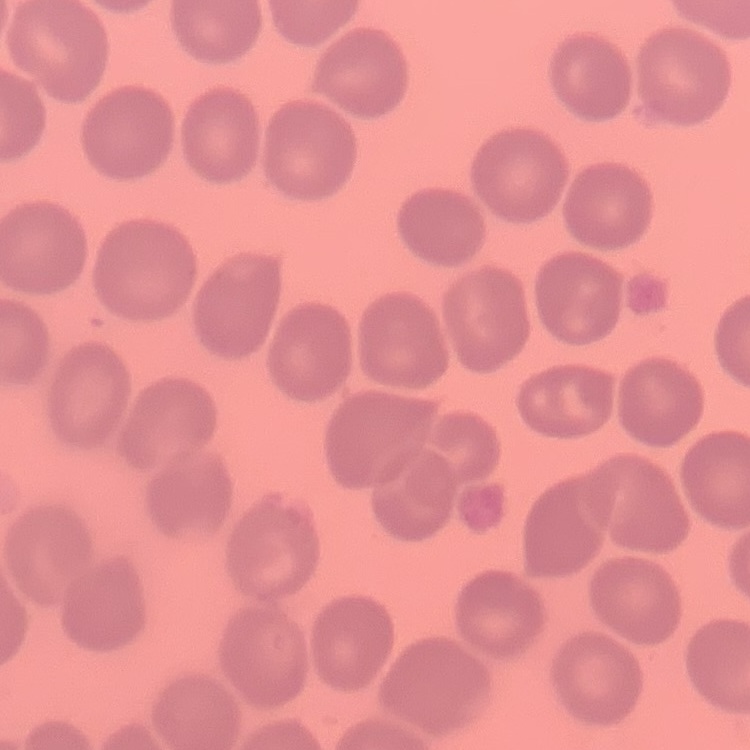
Summary:
  - Red blood cell morphology: no rouleaux formation
  - Stain: Field's or Giemsa
  - Preparation: thin peripheral smear
  - Image type: one tile cut from a larger photomicrograph